Identify the blood parasite species.
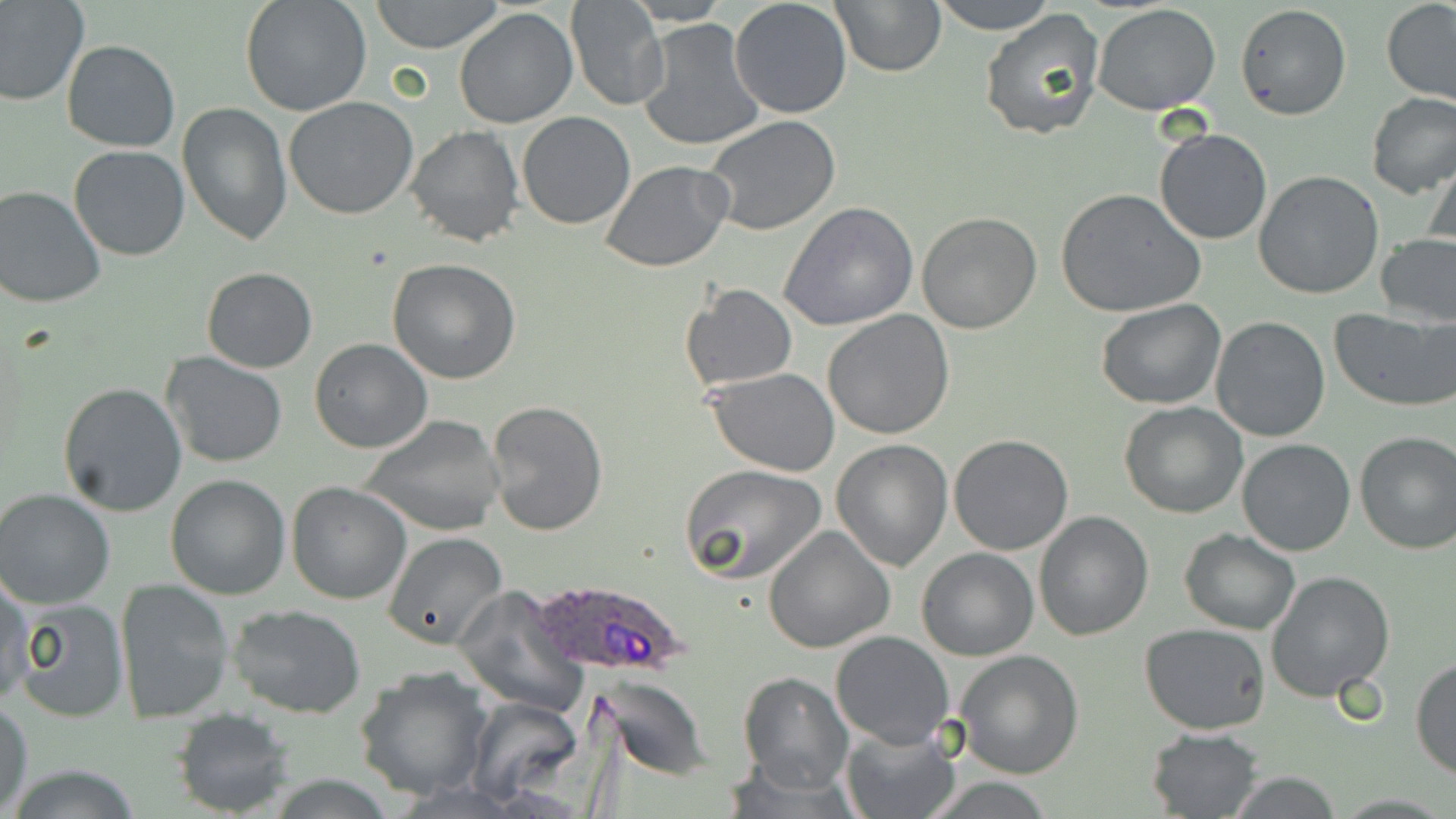
Plasmodium ovale.

Summary:
  - Coordinate format: approximate bounding boxes as [x1, y1, x2, y2] in pixels
  - Plasmodium ovale-infected red blood cell locations: [526, 578, 694, 680]
  - Uninfected red blood cell locations: [0, 0, 90, 106], [240, 0, 373, 118], [370, 0, 504, 53], [729, 0, 853, 118], [828, 0, 946, 77], [927, 0, 1059, 35], [1381, 0, 1456, 104], [565, 1, 670, 113], [1093, 3, 1222, 114], [1235, 3, 1352, 121], [453, 9, 578, 129], [978, 10, 1104, 141], [637, 19, 764, 152], [60, 39, 181, 152], [1366, 91, 1456, 197], [283, 96, 419, 220], [177, 103, 293, 245], [517, 110, 636, 229], [703, 116, 842, 238], [405, 125, 523, 247], [1153, 127, 1273, 245], [68, 145, 193, 262], [1425, 149, 1456, 254], [599, 161, 733, 272], [1254, 169, 1385, 299], [0, 185, 106, 309], [1057, 188, 1208, 319], [780, 203, 921, 333], [915, 211, 1042, 334], [1374, 234, 1456, 328], [387, 257, 521, 384], [202, 266, 317, 373], [678, 284, 798, 392], [1096, 299, 1226, 409], [1329, 308, 1455, 411], [822, 310, 956, 440], [1209, 315, 1330, 442], [310, 340, 433, 453], [162, 353, 289, 470], [707, 367, 843, 475], [57, 382, 188, 518], [485, 400, 609, 538], [1120, 401, 1249, 518], [359, 414, 505, 536], [1353, 431, 1456, 554], [949, 434, 1075, 555], [1237, 438, 1357, 555], [831, 439, 955, 572], [679, 463, 828, 584], [165, 474, 290, 600], [287, 481, 413, 604], [0, 489, 118, 610], [1033, 510, 1154, 641], [763, 524, 896, 653], [1179, 530, 1301, 633], [381, 532, 510, 648], [916, 548, 1038, 661], [0, 569, 32, 705], [1266, 569, 1396, 703], [115, 580, 234, 723], [453, 584, 587, 712], [10, 595, 131, 722], [227, 603, 368, 718], [1140, 624, 1272, 734], [831, 631, 955, 749], [954, 648, 1084, 778], [1412, 657, 1456, 779], [355, 668, 494, 802], [737, 671, 854, 793], [594, 674, 715, 779], [466, 696, 584, 805], [1, 700, 33, 817], [172, 708, 295, 817], [841, 725, 960, 819], [1144, 727, 1263, 818], [6, 765, 148, 819], [1223, 772, 1347, 817]
  - Stain: May-Grünwald-Giemsa
  - Magnification: 1000x
  - Field of view: single
  - Modality: light microscopy
  - Image size: 1456×819 pixels
  - Preparation: thin blood smear